Locate every Plasmodium parasite.
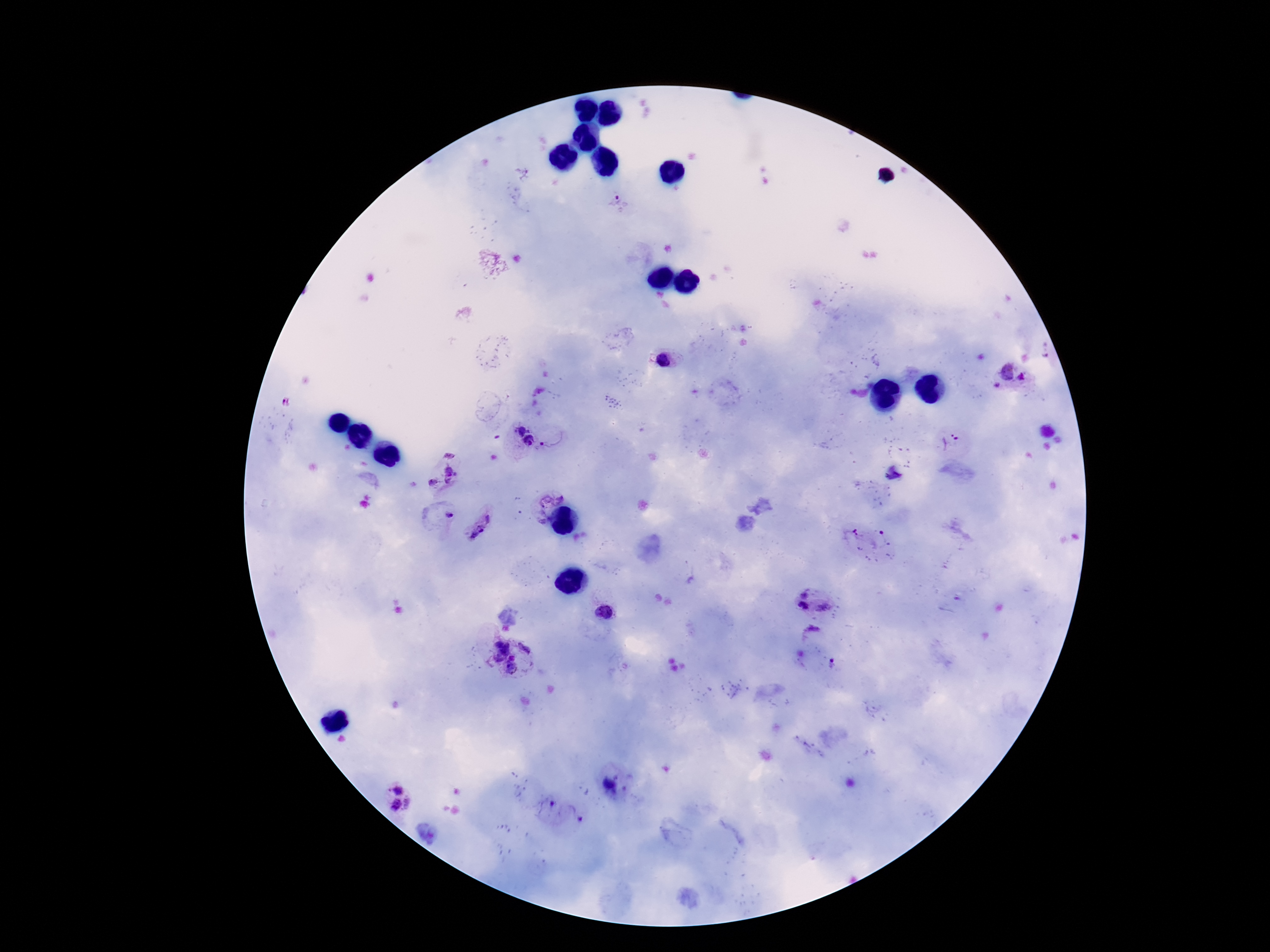

Approximate centers as [x, y] in pixels.
Plasmodium parasites: [663, 360], [1005, 370], [1023, 377], [997, 384], [521, 428], [955, 435], [530, 440], [542, 444], [449, 453], [450, 475], [433, 482], [549, 494], [449, 514], [489, 518], [473, 529], [805, 595], [826, 606], [802, 607], [605, 611], [812, 632], [499, 644], [526, 646], [503, 649], [513, 656], [500, 658], [833, 662], [512, 669], [610, 786], [398, 790], [410, 803], [394, 804].

Summary:
  - Preparation: thick blood smear
  - Capture: smartphone camera through the microscope eyepiece
  - Image size: 1270×952 pixels
  - Patient malaria status: positive
  - Field of view: single
  - Magnification: 100x
  - Stain: Giemsa